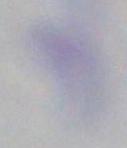
modality: photomicrograph
identification: Toxoplasma gondii
magnification: 1000x